Classify this cell by malaria status.
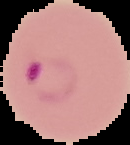

Parasitized.

Image is 130×145 pixels. From a thin blood film. Cell region segmented out of the field of view; the surrounding area is masked to black.